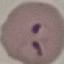

Summary:
  - Malaria status: parasitized
  - Image type: cell patch, automatically extracted from a larger field of view and resized to 64 × 64 pixels
  - Stain: Giemsa
  - Preparation: thin smear
  - Capture: smartphone through the microscope eyepiece